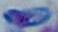

Toxoplasma gondii is shown. Captured at 1000x magnification. Micrograph.